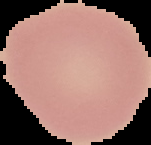
Cell region segmented out of the field of view; the surrounding area is masked to black. Malaria status: uninfected. Image is 151×145 pixels. From a thin blood smear.